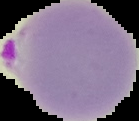
preparation = thin blood smear
image type = segmented cell region on a black background
result = Plasmodium parasites detected
image size = 139×121 pixels